Give the position of every Plasmodium parasite visible.
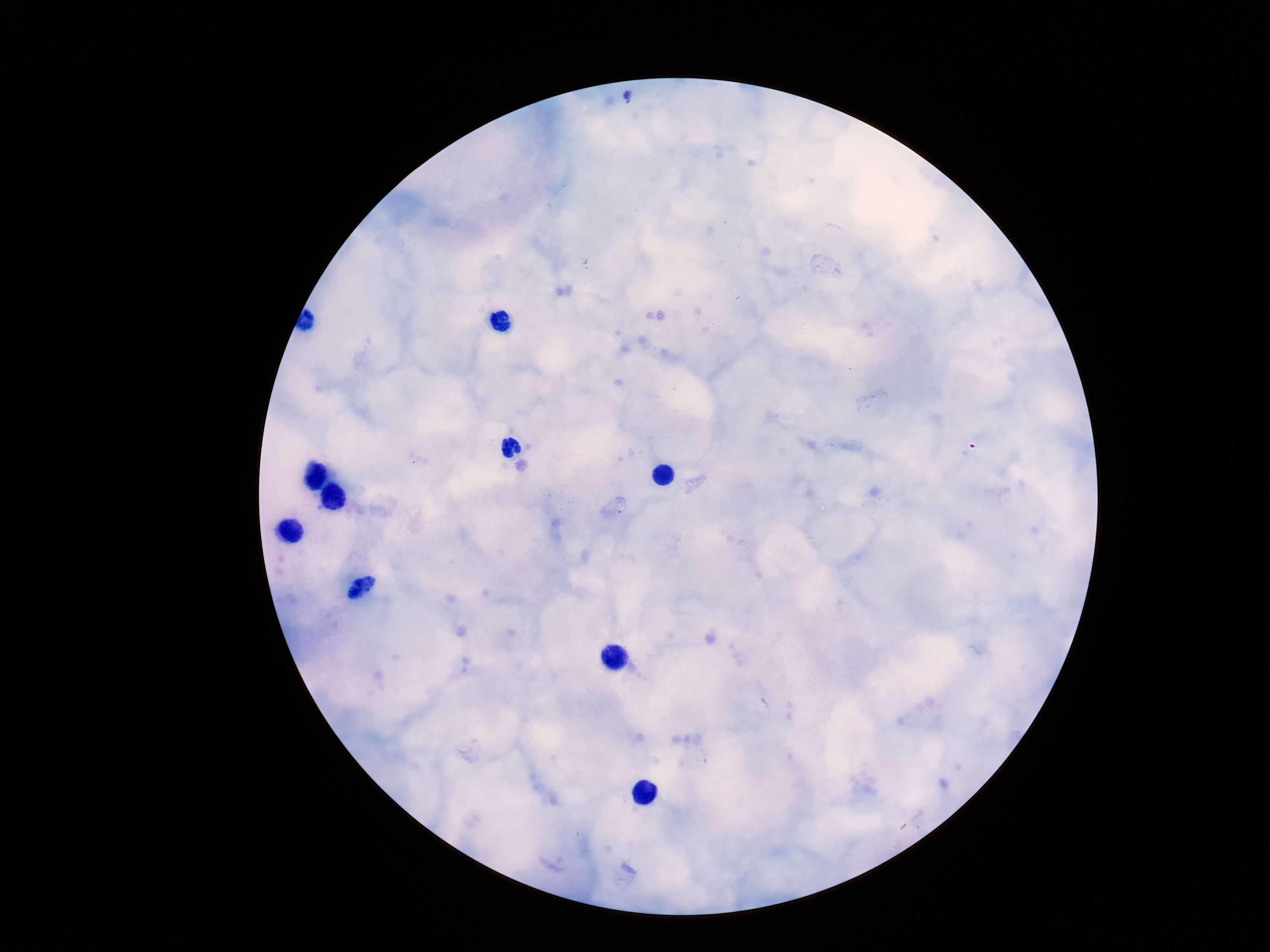

Approximate centers as [x, y] in pixels.
Plasmodium parasites: [631, 98], [620, 505].

Giemsa-stained preparation. 100x magnification. Single field of view. Image is 1270×952 pixels. Photographed through the microscope eyepiece with a smartphone camera. Patient malaria status: positive. Thick blood smear.